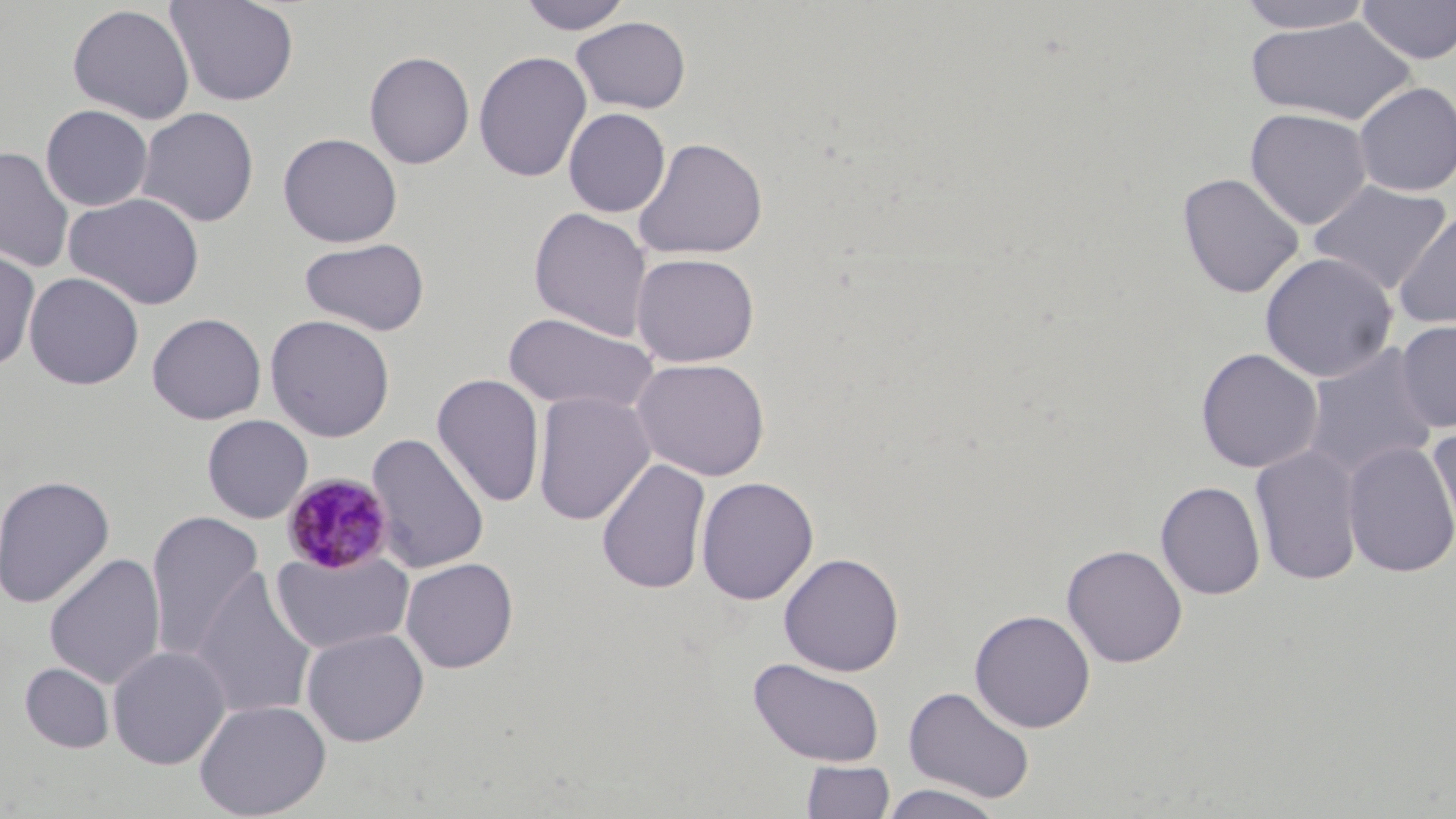

slide-level diagnosis = Plasmodium malariae
uninfected red blood cell locations = approximate bounding boxes as (x1,y1)-(x2,y2) corner pairs in pixels: (165,0)-(300,106), (518,0)-(634,34), (1236,0)-(1377,33), (1357,1)-(1456,64), (67,4)-(195,124), (570,16)-(691,114), (1245,16)-(1418,126), (364,50)-(475,169), (473,51)-(592,183), (1352,81)-(1456,196), (40,104)-(154,212), (135,106)-(259,227), (1245,107)-(1373,230), (563,108)-(671,217), (278,132)-(402,248), (632,137)-(768,260), (0,146)-(76,273), (1176,172)-(1305,299), (1308,180)-(1452,295), (65,192)-(205,310), (528,207)-(653,341), (1393,208)-(1456,331), (299,237)-(430,336), (0,245)-(41,372), (1259,251)-(1399,383), (630,252)-(760,368), (24,272)-(144,390), (146,312)-(266,425), (502,312)-(658,416), (264,314)-(395,442), (1394,319)-(1456,432), (1300,342)-(1439,482), (1195,347)-(1323,473), (631,357)-(771,481), (432,374)-(546,508), (532,391)-(655,526), (202,414)-(313,523), (1428,425)-(1456,547), (365,432)-(490,575), (1341,441)-(1456,578), (1250,445)-(1364,586), (596,458)-(711,594), (0,475)-(115,609), (696,476)-(819,605), (1155,480)-(1266,600), (145,511)-(266,662), (1061,544)-(1188,668), (270,548)-(415,655), (778,552)-(904,677), (44,553)-(166,690), (400,557)-(518,673), (190,567)-(318,722), (970,609)-(1095,732), (301,628)-(429,746), (107,645)-(231,770), (748,657)-(886,767), (20,662)-(114,753), (902,685)-(1036,804), (193,698)-(331,819), (800,760)-(896,819), (878,783)-(1007,819)
stain = May-Grünwald-Giemsa
modality = optical microscopy
Plasmodium malariae-infected red blood cell locations = approximate bounding boxes as (x1,y1)-(x2,y2) corner pairs in pixels: (281,472)-(394,575)
image size = 1456×819 pixels
field of view = one of a larger specimen
preparation = thin blood film
magnification = 1000x